Describe the morphology of the erythrocytes.
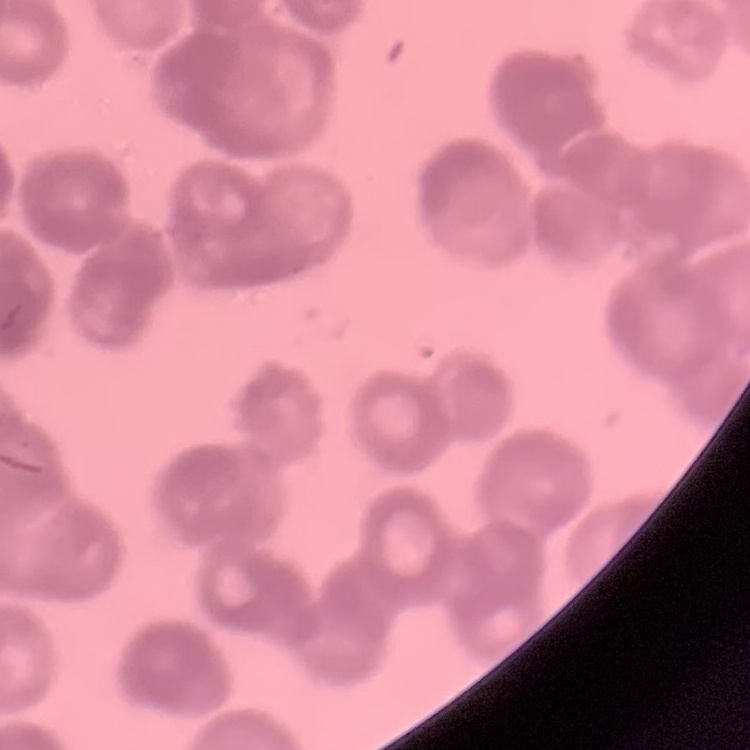
Rouleaux formation.

Summary:
  - Preparation: thin blood film
  - Stain: Field's or Giemsa
  - Image type: one tile cut from a larger photomicrograph